Classify this cell by malaria status.
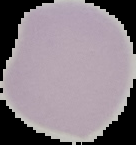

It is uninfected.

preparation = thin blood smear
image size = 136×145 pixels
image type = segmented cell region on a black background